Point out every Plasmodium parasite and every leukocyte.
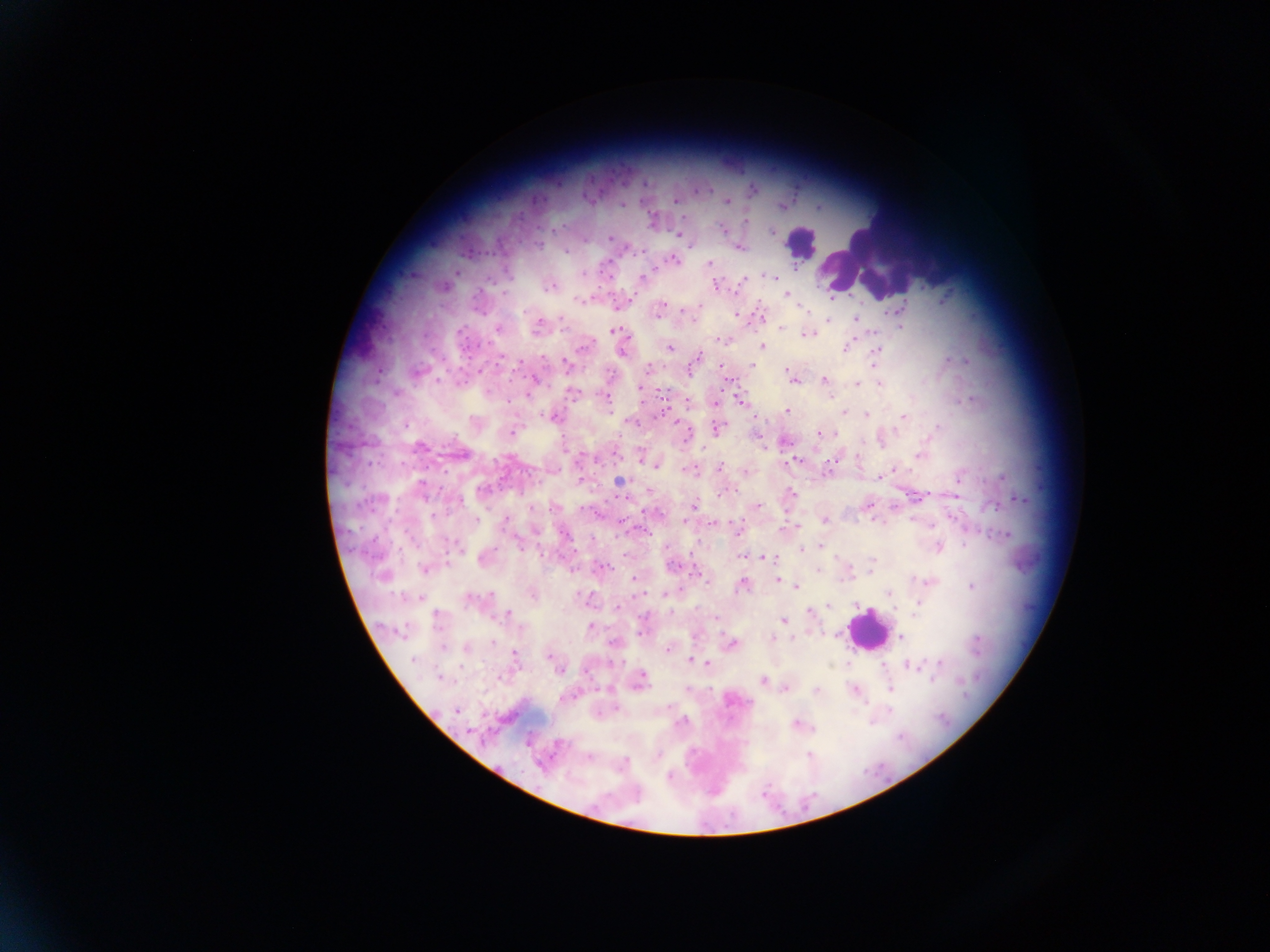
Approximate centers as (x, y) in pixels.
Plasmodium parasites: (751, 189), (675, 201), (726, 201), (622, 204), (782, 206), (819, 207), (686, 218), (652, 220), (745, 220), (725, 231), (771, 231), (679, 235), (610, 238), (691, 244), (738, 247), (565, 250), (642, 250), (673, 259), (710, 263), (455, 272), (608, 273), (583, 274), (774, 276), (642, 278), (742, 279), (716, 284), (550, 286), (442, 287), (788, 294), (582, 300), (698, 304), (617, 306), (902, 306), (802, 307), (886, 311), (735, 313), (658, 314), (762, 316), (562, 319), (855, 319), (828, 320), (693, 321), (537, 326), (497, 328), (780, 328), (900, 328), (616, 331), (806, 334), (724, 340), (762, 346), (670, 347), (846, 347), (875, 351), (622, 352), (696, 358), (948, 360), (965, 360), (566, 364), (752, 365), (721, 367), (647, 368), (377, 369), (416, 372), (793, 378), (823, 380), (533, 381), (856, 384), (879, 384), (639, 387), (571, 392), (528, 393), (607, 397), (740, 399), (972, 399), (687, 402), (715, 403), (788, 411), (843, 412), (867, 415), (552, 416), (902, 416), (756, 417), (632, 423), (677, 424), (716, 429), (512, 432), (820, 432), (783, 441), (421, 446), (764, 449), (459, 453), (640, 455), (919, 456), (793, 460), (657, 464), (719, 467), (690, 470), (892, 470), (745, 472), (827, 472), (878, 476), (1002, 476), (618, 480), (580, 481), (649, 490), (719, 493), (792, 495), (954, 495), (626, 497), (1018, 498), (695, 504), (867, 505), (756, 506), (554, 507), (872, 518), (824, 520), (913, 520), (505, 521), (685, 521), (713, 523), (797, 528), (736, 529), (645, 531), (1005, 534), (458, 547), (822, 547), (937, 547), (801, 549), (742, 556), (763, 556), (484, 558), (871, 561), (672, 565), (602, 567), (425, 568), (817, 569), (869, 572), (697, 573), (384, 575), (634, 578), (777, 579), (708, 581), (929, 581), (743, 584), (797, 585), (972, 586), (890, 592), (666, 593), (532, 594), (471, 599), (586, 599), (829, 605), (616, 607), (808, 613), (508, 614), (716, 617), (784, 620), (589, 627), (641, 632), (900, 637), (772, 638), (731, 644), (466, 646), (667, 649), (515, 654), (550, 654), (692, 661), (939, 663), (708, 664), (911, 665), (558, 669), (440, 678), (762, 680), (639, 681), (785, 688), (890, 688), (687, 689), (854, 689), (816, 691), (614, 708), (456, 709), (682, 721), (797, 724), (588, 757).
Leukocytes: (803, 243), (869, 256), (867, 630).

image_size: 1270×952 pixels
country: Ghana
preparation: thick blood smear
capture: mobile-phone photograph through a microscope
field_of_view: single